Point out each Plasmodium parasite.
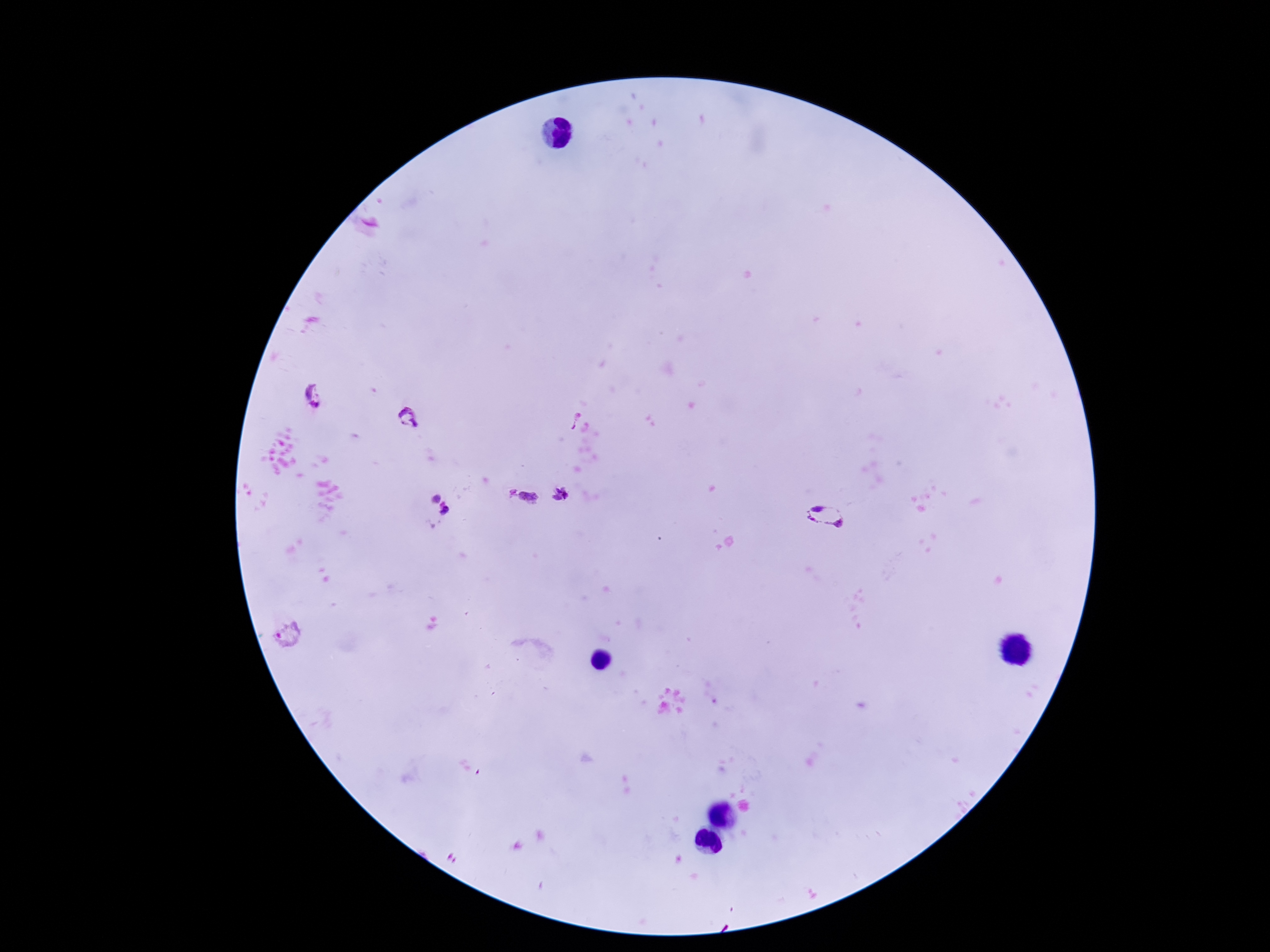

Approximate centers as (x, y) in pixels.
Plasmodium parasites: (315, 396), (409, 418), (572, 418), (512, 494), (561, 495), (528, 497), (437, 499), (446, 511), (826, 516), (291, 636).

stain = Giemsa
capture = smartphone camera through the microscope eyepiece
magnification = 100x
preparation = thick blood film
image size = 1270×952 pixels
patient malaria status = positive
field of view = single